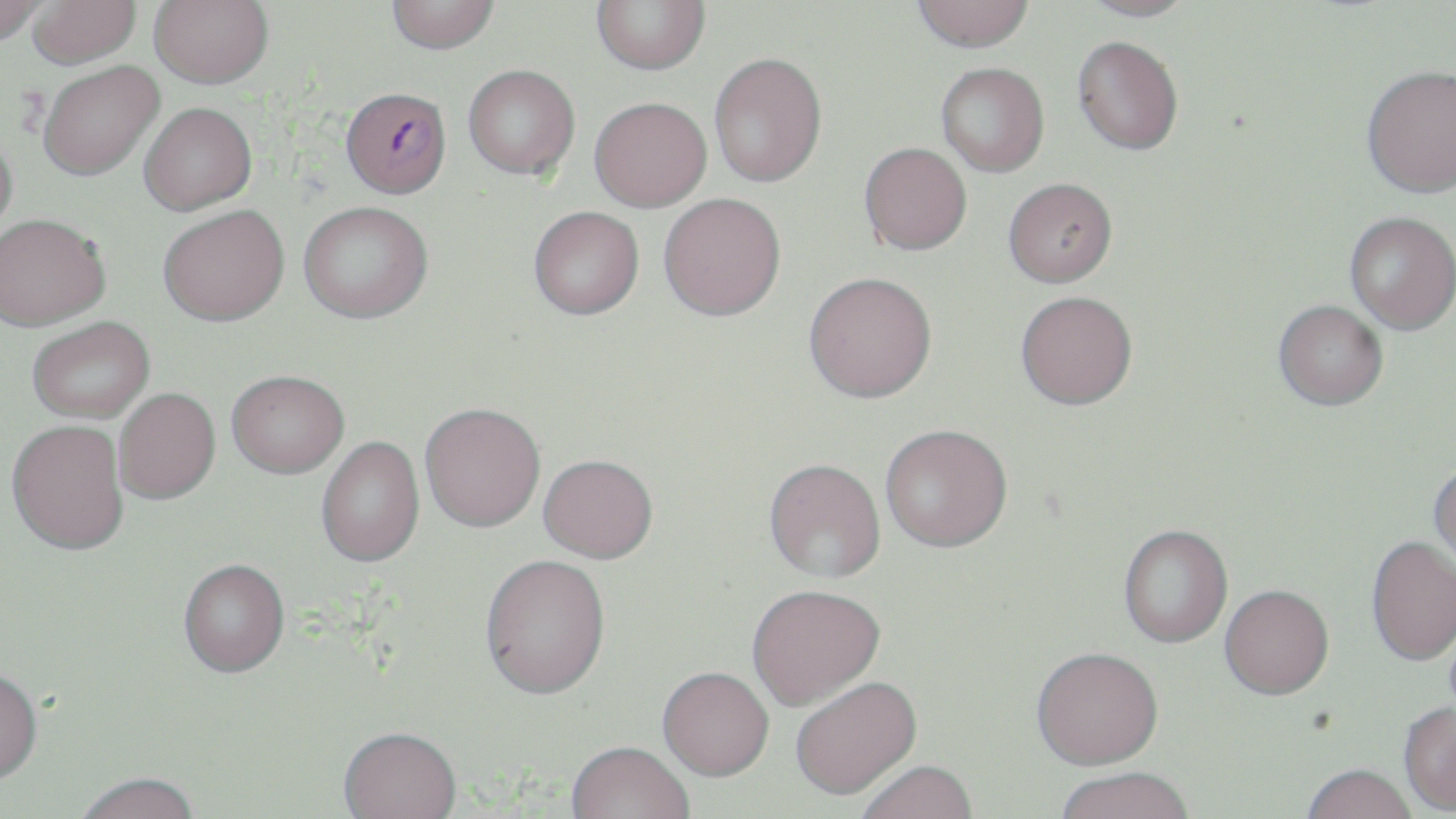
Summary:
  - Coordinate format: approximate bounding boxes as named x1/y1/x2/y2 corners in pixels
  - Plasmodium falciparum-infected red blood cell locations: (x1=341, y1=86, x2=451, y2=198)
  - Uninfected red blood cell locations: (x1=0, y1=0, x2=49, y2=46), (x1=149, y1=0, x2=274, y2=88), (x1=386, y1=0, x2=499, y2=54), (x1=591, y1=0, x2=710, y2=74), (x1=912, y1=0, x2=1036, y2=52), (x1=1079, y1=0, x2=1199, y2=21), (x1=28, y1=1, x2=141, y2=68), (x1=1073, y1=35, x2=1184, y2=155), (x1=708, y1=51, x2=827, y2=187), (x1=38, y1=61, x2=163, y2=180), (x1=936, y1=62, x2=1049, y2=177), (x1=463, y1=64, x2=580, y2=179), (x1=1362, y1=64, x2=1456, y2=198), (x1=589, y1=97, x2=711, y2=212), (x1=138, y1=102, x2=257, y2=215), (x1=0, y1=129, x2=18, y2=240), (x1=859, y1=142, x2=972, y2=255), (x1=1003, y1=177, x2=1117, y2=288), (x1=658, y1=192, x2=786, y2=320), (x1=298, y1=201, x2=433, y2=322), (x1=158, y1=204, x2=289, y2=326), (x1=528, y1=206, x2=644, y2=319), (x1=1344, y1=211, x2=1455, y2=334), (x1=0, y1=213, x2=110, y2=330), (x1=803, y1=271, x2=936, y2=402), (x1=1015, y1=290, x2=1138, y2=410), (x1=1273, y1=300, x2=1388, y2=411), (x1=27, y1=316, x2=154, y2=423), (x1=226, y1=369, x2=349, y2=477), (x1=113, y1=387, x2=220, y2=504), (x1=419, y1=402, x2=545, y2=532), (x1=7, y1=419, x2=129, y2=555), (x1=880, y1=427, x2=1012, y2=555), (x1=316, y1=436, x2=424, y2=569), (x1=538, y1=456, x2=658, y2=565), (x1=764, y1=461, x2=885, y2=586), (x1=1428, y1=462, x2=1456, y2=572), (x1=1118, y1=527, x2=1233, y2=650), (x1=1365, y1=535, x2=1456, y2=667), (x1=480, y1=557, x2=611, y2=705), (x1=178, y1=561, x2=289, y2=680), (x1=1219, y1=587, x2=1334, y2=704), (x1=747, y1=588, x2=885, y2=714), (x1=1031, y1=651, x2=1165, y2=775), (x1=657, y1=671, x2=773, y2=785), (x1=0, y1=673, x2=43, y2=788), (x1=791, y1=679, x2=923, y2=803), (x1=1398, y1=703, x2=1456, y2=816), (x1=338, y1=731, x2=461, y2=819), (x1=565, y1=745, x2=694, y2=819), (x1=856, y1=764, x2=978, y2=819), (x1=1301, y1=768, x2=1417, y2=819), (x1=1055, y1=772, x2=1195, y2=819), (x1=76, y1=775, x2=200, y2=819)
  - Slide-level diagnosis: Plasmodium falciparum
  - Image size: 1456×819 pixels
  - Field of view: one of a larger specimen
  - Stain: May-Grünwald-Giemsa
  - Magnification: 1000x
  - Preparation: thin blood smear
  - Modality: optical microscopy